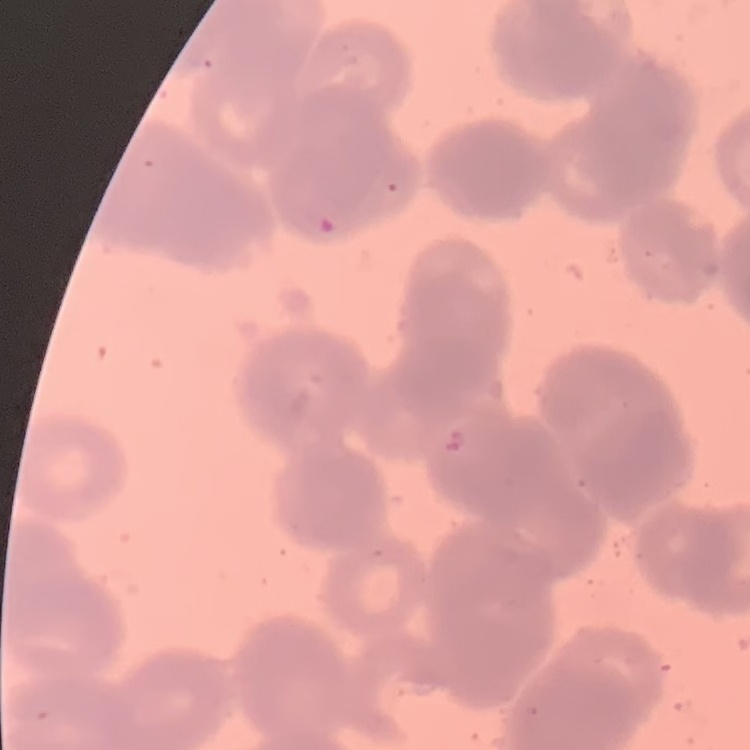

The erythrocytes show rouleaux formation. One tile cut from a larger photomicrograph. Stained with either Field's or Giemsa. Thin peripheral smear.